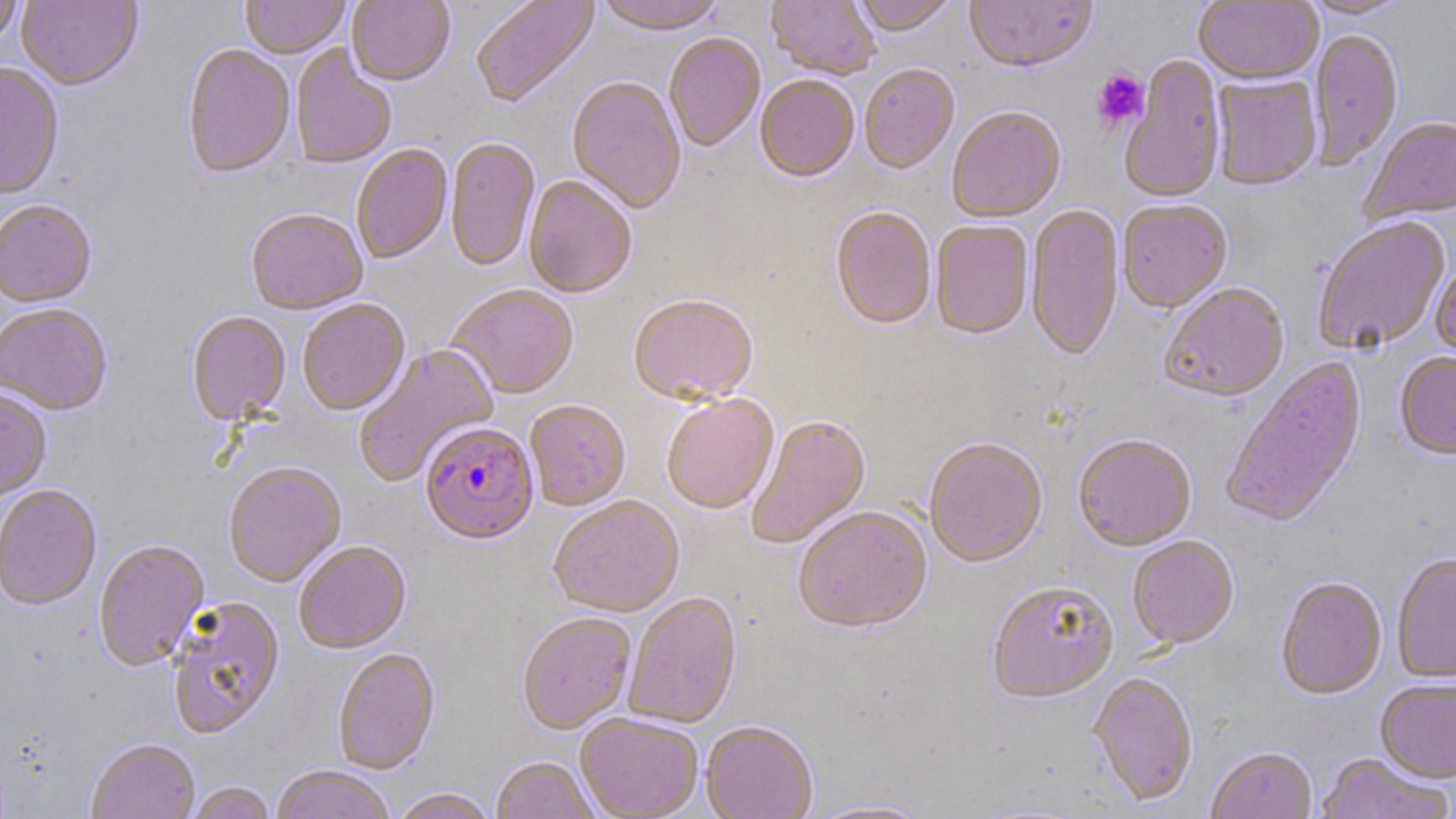
Approximate bounding boxes as [x1, y1, x2, y2] in pixels. Plasmodium falciparum-infected red blood cell locations: [420, 423, 539, 549]. Uninfected red blood cell locations: [0, 0, 24, 50], [16, 0, 143, 92], [240, 0, 350, 60], [346, 0, 454, 88], [470, 0, 600, 110], [594, 0, 726, 38], [766, 0, 879, 81], [851, 0, 961, 38], [964, 0, 1099, 75], [1299, 0, 1413, 21], [1194, 1, 1322, 88], [1309, 29, 1403, 172], [664, 34, 765, 153], [182, 45, 295, 182], [290, 45, 396, 171], [1118, 56, 1226, 206], [0, 65, 64, 201], [859, 66, 960, 176], [1210, 75, 1322, 193], [755, 76, 859, 185], [567, 78, 686, 216], [947, 108, 1067, 225], [1360, 118, 1456, 225], [445, 139, 540, 273], [352, 144, 453, 265], [523, 177, 636, 300], [0, 201, 97, 310], [1117, 201, 1232, 315], [1026, 205, 1125, 364], [829, 207, 936, 333], [245, 211, 368, 317], [1312, 218, 1452, 355], [930, 222, 1034, 341], [1430, 261, 1456, 366], [1159, 285, 1290, 405], [446, 287, 579, 401], [628, 296, 758, 408], [297, 300, 410, 417], [0, 306, 112, 418], [186, 313, 291, 427], [352, 344, 499, 488], [1394, 354, 1456, 462], [1220, 357, 1369, 531], [0, 390, 52, 503], [661, 396, 779, 516], [525, 402, 631, 513], [746, 416, 871, 550], [1073, 436, 1197, 554], [924, 440, 1048, 570], [223, 464, 346, 589], [0, 487, 102, 613], [548, 497, 685, 619], [793, 509, 932, 636], [1127, 537, 1239, 652], [94, 541, 210, 673], [295, 543, 411, 656], [1391, 555, 1456, 685], [1276, 578, 1387, 701], [988, 584, 1118, 707], [624, 594, 743, 729], [166, 597, 286, 742], [517, 614, 636, 736], [333, 650, 441, 776], [1088, 673, 1199, 808], [1375, 680, 1455, 786], [576, 714, 703, 819], [701, 723, 818, 819], [86, 741, 200, 819], [1206, 748, 1317, 819], [1315, 753, 1453, 819], [490, 758, 601, 819], [270, 767, 395, 819], [184, 782, 275, 818], [390, 788, 498, 819], [799, 798, 936, 818]. Platelet locations: [1091, 69, 1149, 131]. Slide-level diagnosis: Plasmodium falciparum. One field of a larger specimen. 1000x magnification. Image is 1456×819 pixels. Thin blood film. May-Grünwald-Giemsa stain. Light microscopy.